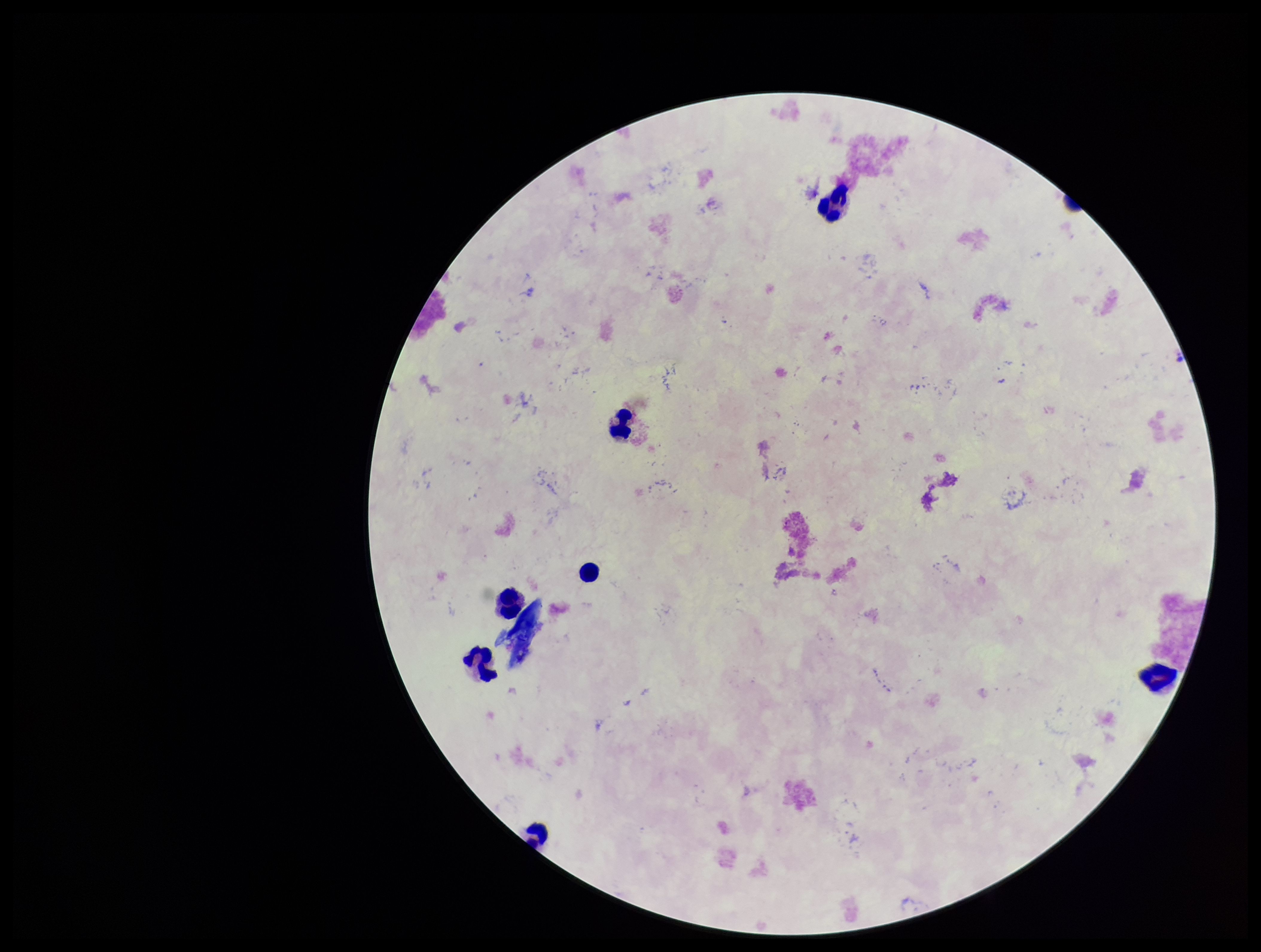
image size = 1261×952 pixels
capture = smartphone photograph through the microscope eyepiece
Plasmodium parasites = none seen
leukocyte count = 7
stain = Giemsa
preparation = thick
parasite count = 0
patient malaria status = negative
field of view = one from this slide